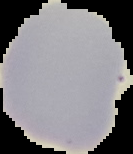

Summary:
  - Image size: 133×154 pixels
  - Preparation: thin blood film
  - Result: no Plasmodium parasites detected
  - Image type: cell region segmented out of the field of view; surrounding area masked to black